Identify the blood parasite species.
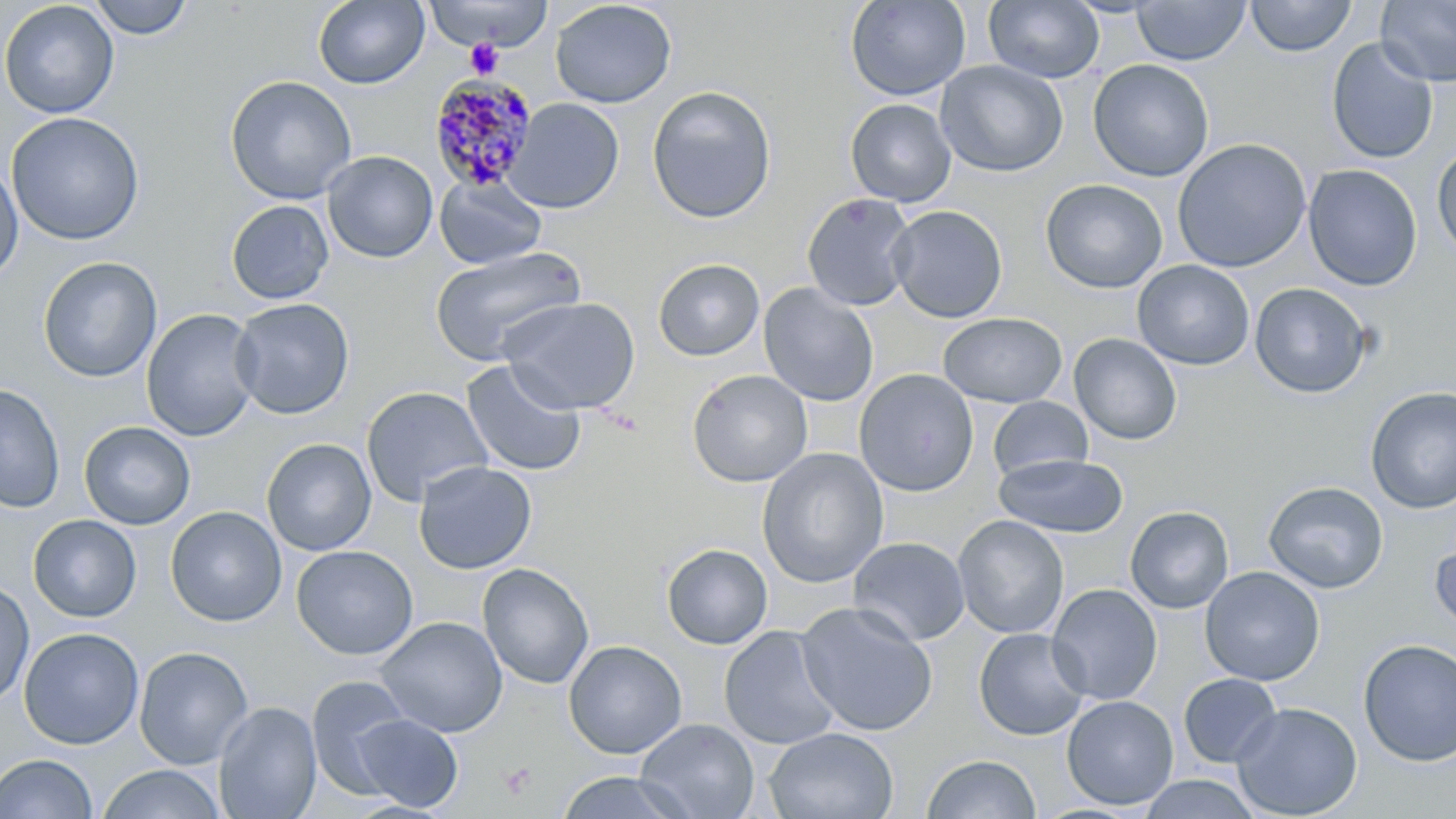
Plasmodium malariae.

uninfected red blood cell locations = approximate bounding boxes as (x1,y1)-(x2,y2) corner pairs in pixels: (88,0)-(195,40), (845,0)-(970,101), (1246,0)-(1356,57), (1376,0)-(1456,86), (0,1)-(119,119), (313,1)-(429,89), (423,1)-(554,51), (550,1)-(677,108), (984,1)-(1104,84), (1131,1)-(1250,66), (1325,38)-(1439,165), (1087,59)-(1214,182), (936,60)-(1068,178), (224,75)-(358,205), (647,85)-(777,223), (506,98)-(624,213), (845,98)-(957,207), (6,112)-(145,245), (1172,138)-(1311,273), (1432,146)-(1456,259), (322,151)-(438,263), (0,159)-(23,286), (1303,164)-(1422,291), (433,174)-(547,269), (1040,179)-(1168,294), (802,192)-(917,311), (226,200)-(334,304), (887,205)-(1008,323), (429,245)-(588,366), (38,256)-(162,383), (652,258)-(765,361), (1132,260)-(1254,370), (1249,282)-(1371,398), (758,283)-(879,407), (500,296)-(640,414), (229,297)-(354,419), (141,308)-(261,442), (937,312)-(1067,407), (1069,333)-(1182,446), (461,359)-(588,478), (853,368)-(979,497), (687,369)-(812,487), (0,384)-(65,514), (360,385)-(494,507), (1365,387)-(1456,513), (988,397)-(1092,481), (79,421)-(196,529), (261,438)-(377,556), (756,447)-(888,588), (993,454)-(1128,538), (413,461)-(537,574), (1264,481)-(1388,593), (166,506)-(287,627), (1125,506)-(1234,614), (28,515)-(142,622), (953,515)-(1069,639), (848,537)-(970,645), (1430,537)-(1456,636), (661,543)-(772,649), (291,545)-(418,660), (477,562)-(594,690), (1199,566)-(1325,686), (0,580)-(34,708), (1047,584)-(1163,706), (796,602)-(939,737), (376,616)-(508,737), (719,625)-(841,750), (18,627)-(144,749), (973,628)-(1091,740), (1357,639)-(1456,766), (563,640)-(687,759), (134,646)-(254,769), (1178,673)-(1283,768), (306,674)-(413,796), (1061,695)-(1179,810), (214,701)-(322,819), (1230,702)-(1362,818), (351,713)-(463,812), (636,718)-(759,819), (764,727)-(899,818), (0,753)-(97,819), (922,754)-(1040,818), (98,764)-(225,819), (555,771)-(691,819), (1137,775)-(1261,818)
Plasmodium malariae-infected red blood cell locations = approximate bounding boxes as (x1,y1)-(x2,y2) corner pairs in pixels: (429,76)-(539,194)
platelet locations = approximate bounding boxes as (x1,y1)-(x2,y2) corner pairs in pixels: (465,39)-(505,80), (598,408)-(645,436), (497,762)-(538,800)
preparation = thin blood film
magnification = 1000x
modality = light microscopy
image size = 1456×819 pixels
field of view = one of a larger specimen
stain = May-Grünwald-Giemsa